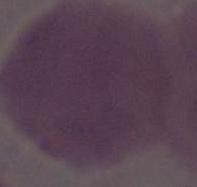

modality = micrograph
magnification = 1000x
identification = erythrocyte